Name the parasite shown.
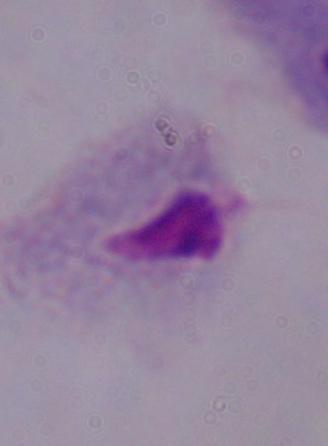

A trichomonad.

magnification = 1000x
modality = photomicrograph